Assess this cell for malaria.
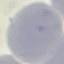

Uninfected.

image type = cell patch, automatically extracted from a larger field of view and resized to 64 × 64 pixels
stain = Giemsa
preparation = thin smear
capture = smartphone through the microscope eyepiece